Identify the parasite.
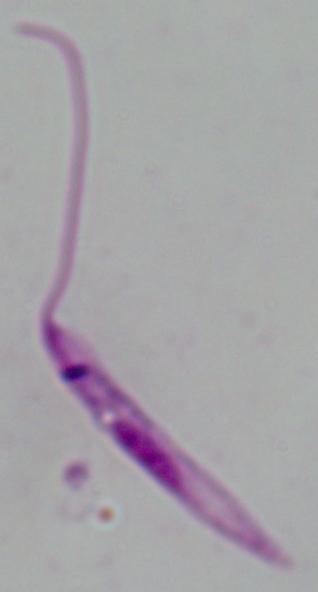
This is Leishmania.

Summary:
  - Modality: micrograph
  - Magnification: 1000x